Identify the cell.
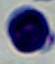
This is a leukocyte.

modality = micrograph
magnification = 1000x